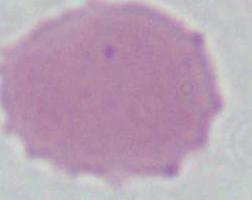
magnification = 1000x
identification = red blood cell
modality = photomicrograph